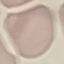
{
  "malaria_status": "uninfected",
  "stain": "Giemsa",
  "image_type": "automatically extracted cell patch, resized to 64 × 64 pixels",
  "preparation": "thin blood film",
  "capture": "smartphone through the microscope eyepiece"
}